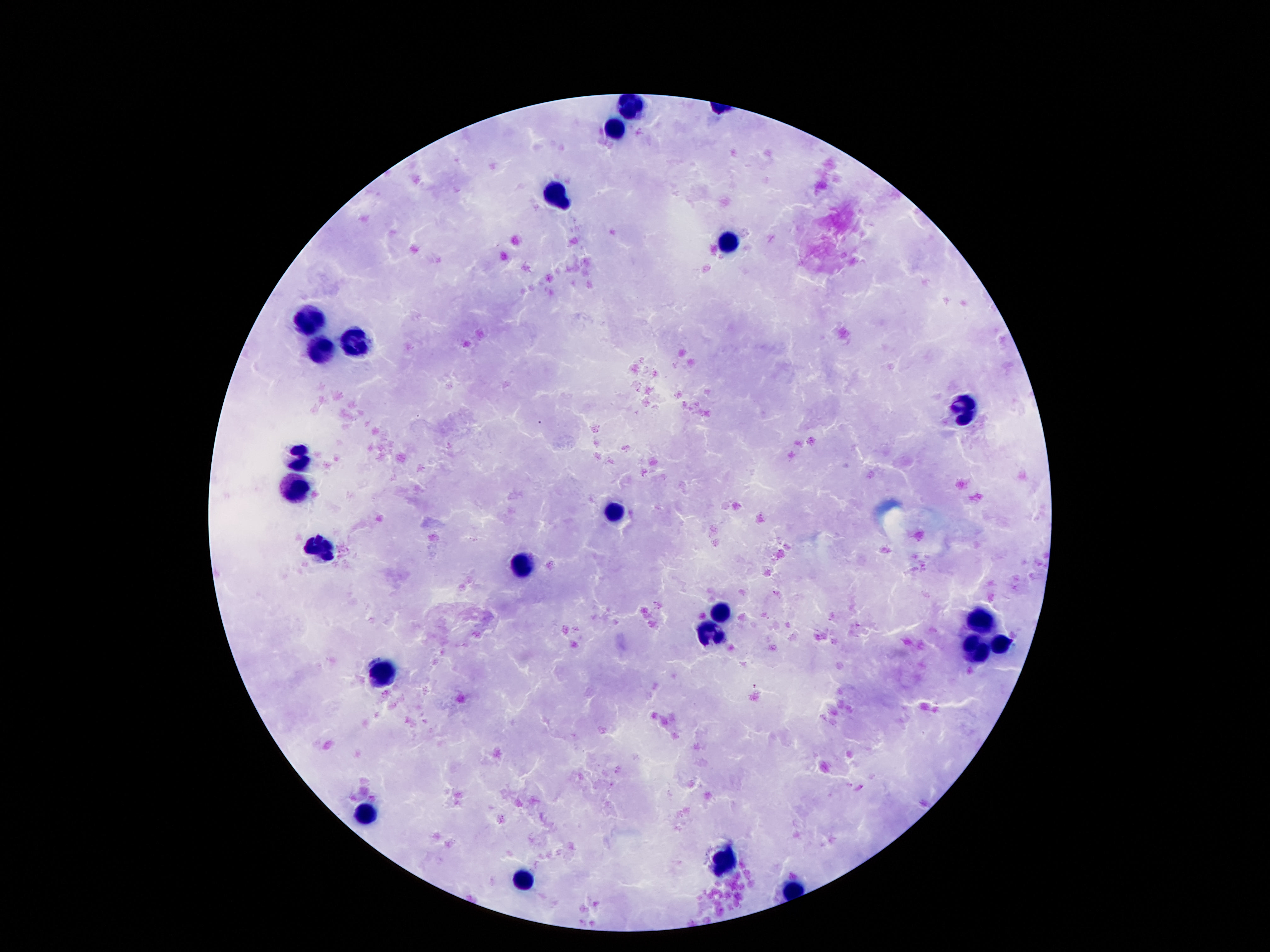

Approximate centers as [x, y] in pixels.
Summary:
  - Leukocyte locations: [632, 107], [615, 129], [558, 195], [726, 242], [311, 320], [361, 342], [320, 352], [967, 409], [298, 459], [295, 488], [615, 512], [322, 547], [526, 568], [723, 612], [980, 620], [708, 630], [1001, 644], [973, 648], [385, 675], [366, 815], [724, 860], [526, 880]
  - Magnification: 100x
  - Field of view: one from this slide
  - Preparation: thick blood film
  - Patient malaria status: not infected
  - Image size: 1270×952 pixels
  - Stain: Giemsa
  - Capture: smartphone camera through the microscope eyepiece